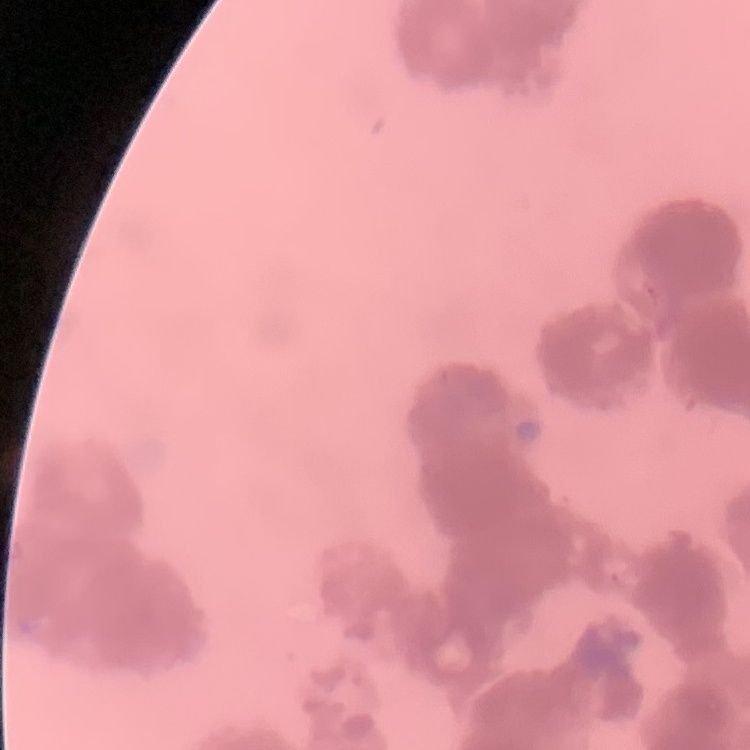 The red blood cells exhibit rouleaux formation. Stained with either Field's or Giemsa. One tile cut from a larger photomicrograph. Thin peripheral smear.